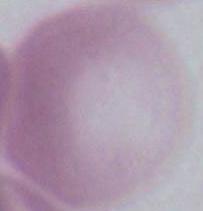 A red blood cell is shown. Micrograph. 1000x magnification.